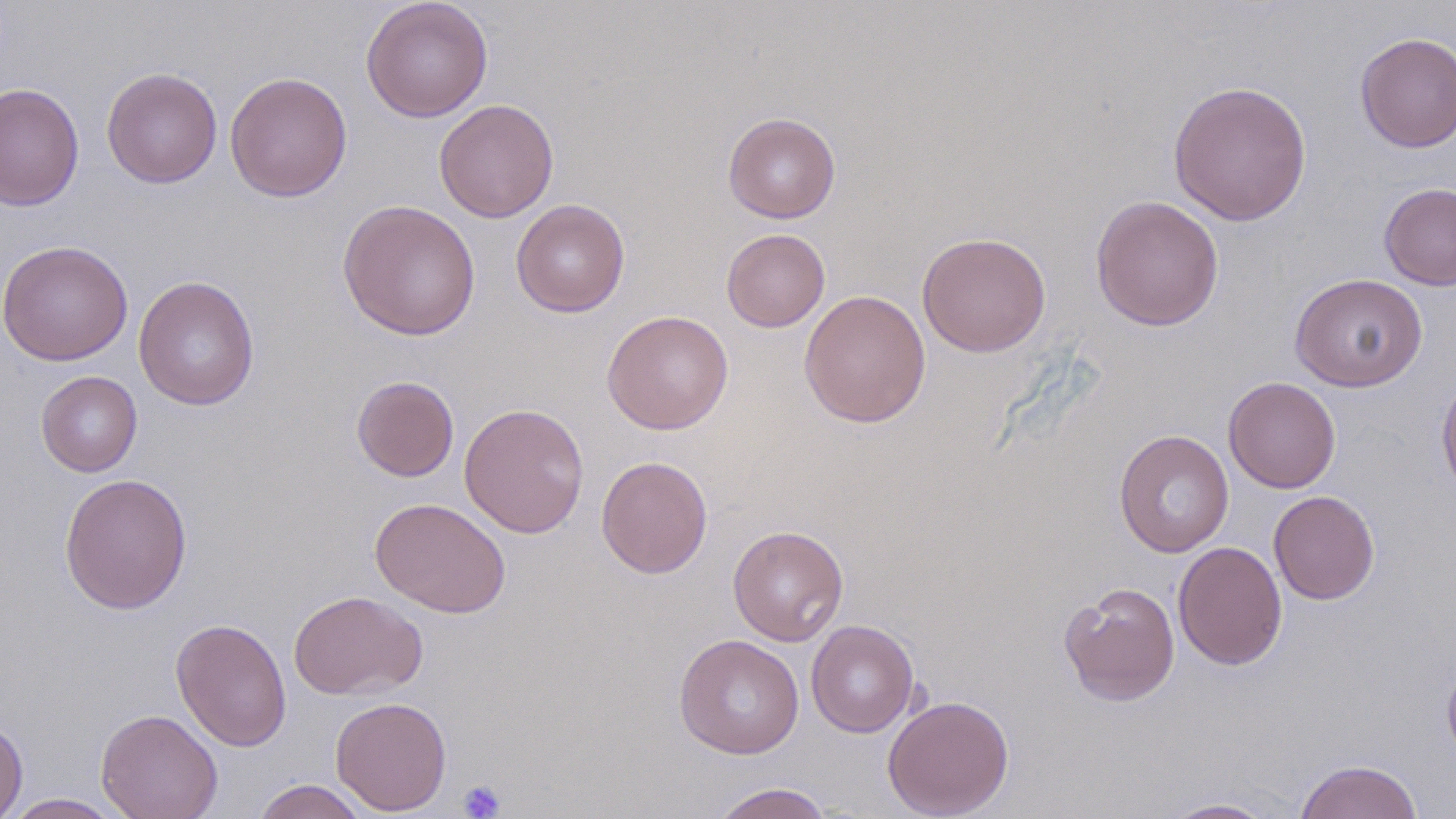
Summary:
  - Coordinate format: approximate bounding boxes as [x1, y1, x2, y2] in pixels
  - Platelet locations: [457, 780, 506, 818]
  - Uninfected red blood cell locations: [360, 0, 493, 123], [1355, 32, 1456, 153], [101, 67, 223, 188], [225, 71, 352, 202], [1168, 79, 1312, 226], [0, 82, 85, 212], [434, 99, 559, 223], [722, 112, 841, 223], [1378, 182, 1456, 291], [1090, 195, 1224, 331], [511, 198, 630, 317], [337, 199, 481, 341], [721, 228, 830, 332], [916, 231, 1051, 357], [0, 240, 133, 365], [1289, 272, 1428, 392], [133, 275, 260, 410], [799, 289, 931, 429], [602, 310, 734, 435], [36, 370, 143, 477], [1436, 370, 1456, 500], [351, 375, 459, 482], [1223, 376, 1340, 493], [459, 403, 590, 538], [1114, 429, 1234, 557], [596, 456, 713, 579], [59, 471, 193, 615], [1269, 490, 1379, 605], [370, 497, 511, 618], [727, 524, 849, 646], [1173, 541, 1287, 670], [1058, 581, 1180, 706], [288, 590, 427, 699], [170, 618, 292, 752], [806, 620, 919, 738], [674, 634, 804, 759], [1442, 655, 1456, 768], [882, 695, 1014, 818], [330, 696, 452, 815], [96, 709, 223, 819], [0, 717, 28, 819], [1294, 759, 1423, 819], [251, 779, 370, 818], [708, 782, 835, 819], [1, 793, 129, 818], [1159, 797, 1280, 818]
  - Slide-level diagnosis: negative for blood parasites
  - Modality: light microscopy
  - Image size: 1456×819 pixels
  - Field of view: single
  - Stain: May-Grünwald-Giemsa
  - Magnification: 1000x
  - Preparation: thin blood film